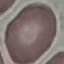

malaria status = uninfected
capture = smartphone through the microscope eyepiece
stain = Giemsa
image type = automatically extracted cell patch, resized to 64 × 64 pixels
preparation = thin smear